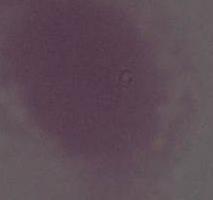

Summary:
  - Identification: red blood cell
  - Modality: micrograph
  - Magnification: 1000x